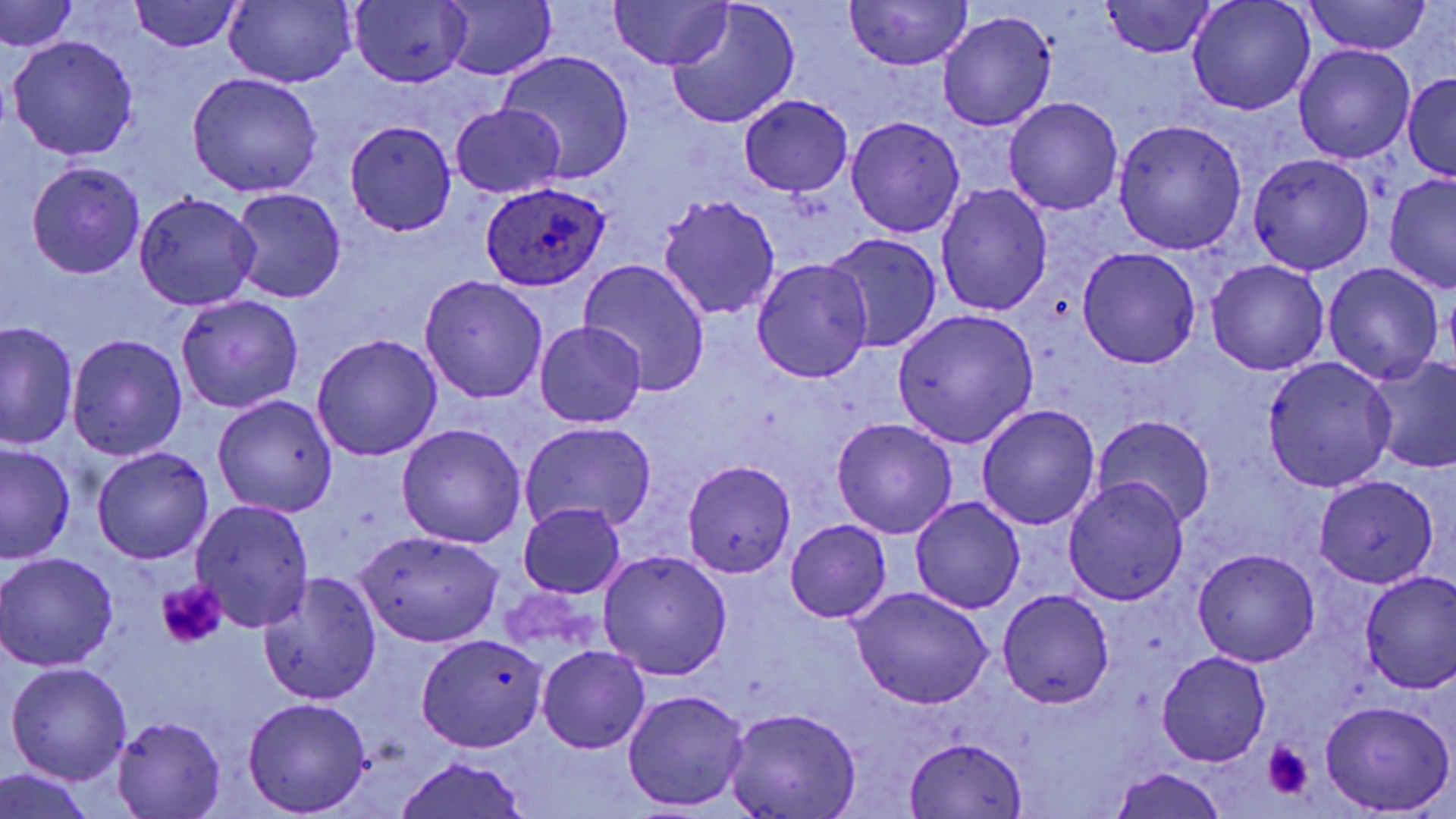

Approximate bounding boxes as named x1/y1/x2/y2 corners in pixels. Platelet locations: (x1=155, y1=579, x2=227, y2=650), (x1=1262, y1=743, x2=1313, y2=800). Plasmodium ovale-infected red blood cell locations: (x1=481, y1=181, x2=609, y2=290). Uninfected red blood cell locations: (x1=609, y1=0, x2=730, y2=71), (x1=844, y1=0, x2=970, y2=72), (x1=1186, y1=0, x2=1317, y2=116), (x1=1, y1=1, x2=78, y2=54), (x1=129, y1=1, x2=242, y2=52), (x1=347, y1=1, x2=472, y2=88), (x1=1102, y1=1, x2=1218, y2=58), (x1=1303, y1=1, x2=1433, y2=56), (x1=224, y1=2, x2=354, y2=87), (x1=666, y1=2, x2=800, y2=129), (x1=438, y1=3, x2=556, y2=80), (x1=938, y1=12, x2=1055, y2=130), (x1=7, y1=35, x2=140, y2=160), (x1=1293, y1=46, x2=1416, y2=164), (x1=498, y1=51, x2=635, y2=183), (x1=187, y1=72, x2=323, y2=196), (x1=1403, y1=73, x2=1456, y2=179), (x1=740, y1=95, x2=853, y2=197), (x1=1003, y1=97, x2=1124, y2=217), (x1=450, y1=104, x2=566, y2=199), (x1=846, y1=115, x2=966, y2=238), (x1=1113, y1=119, x2=1247, y2=254), (x1=344, y1=120, x2=457, y2=235), (x1=1248, y1=154, x2=1374, y2=276), (x1=26, y1=160, x2=145, y2=278), (x1=1383, y1=174, x2=1456, y2=293), (x1=936, y1=183, x2=1053, y2=317), (x1=229, y1=187, x2=346, y2=305), (x1=133, y1=193, x2=260, y2=310), (x1=657, y1=196, x2=782, y2=320), (x1=826, y1=233, x2=941, y2=354), (x1=1076, y1=247, x2=1201, y2=369), (x1=579, y1=258, x2=713, y2=396), (x1=751, y1=258, x2=875, y2=383), (x1=1206, y1=259, x2=1329, y2=376), (x1=1323, y1=264, x2=1444, y2=384), (x1=419, y1=276, x2=548, y2=403), (x1=176, y1=294, x2=304, y2=414), (x1=892, y1=308, x2=1039, y2=449), (x1=536, y1=321, x2=647, y2=428), (x1=2, y1=322, x2=77, y2=451), (x1=66, y1=334, x2=189, y2=460), (x1=312, y1=335, x2=441, y2=461), (x1=1263, y1=356, x2=1398, y2=490), (x1=1367, y1=357, x2=1456, y2=476), (x1=213, y1=394, x2=339, y2=518), (x1=976, y1=404, x2=1101, y2=531), (x1=1093, y1=413, x2=1216, y2=529), (x1=831, y1=417, x2=958, y2=539), (x1=520, y1=421, x2=657, y2=534), (x1=396, y1=424, x2=526, y2=548), (x1=0, y1=444, x2=75, y2=564), (x1=91, y1=447, x2=214, y2=564), (x1=682, y1=459, x2=796, y2=577), (x1=1315, y1=475, x2=1440, y2=588), (x1=1064, y1=478, x2=1188, y2=605), (x1=910, y1=495, x2=1025, y2=614), (x1=190, y1=499, x2=315, y2=632), (x1=517, y1=504, x2=627, y2=598), (x1=786, y1=519, x2=890, y2=622), (x1=354, y1=530, x2=505, y2=648), (x1=1193, y1=547, x2=1320, y2=667), (x1=0, y1=552, x2=120, y2=671), (x1=599, y1=552, x2=732, y2=681), (x1=255, y1=569, x2=383, y2=704), (x1=1359, y1=571, x2=1456, y2=695), (x1=849, y1=588, x2=992, y2=709), (x1=998, y1=589, x2=1115, y2=708), (x1=415, y1=633, x2=547, y2=752), (x1=538, y1=645, x2=651, y2=753), (x1=1155, y1=651, x2=1272, y2=766), (x1=5, y1=662, x2=132, y2=784), (x1=622, y1=688, x2=749, y2=811), (x1=242, y1=697, x2=373, y2=815), (x1=1319, y1=700, x2=1454, y2=815), (x1=723, y1=709, x2=862, y2=819), (x1=112, y1=715, x2=226, y2=819), (x1=906, y1=737, x2=1028, y2=817), (x1=393, y1=756, x2=532, y2=819), (x1=1110, y1=766, x2=1228, y2=819), (x1=0, y1=769, x2=94, y2=819). Slide-level diagnosis: Plasmodium ovale. Image is 1456×819 pixels. Captured at 1000x magnification. Thin blood smear. Optical microscopy. May-Grünwald-Giemsa stain. Single field of view.